Report the malaria status of this cell.
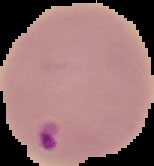
Parasitized.

preparation: thin blood film
image_type: cell region segmented out of the field of view; surrounding area masked to black
image_size: 154×166 pixels